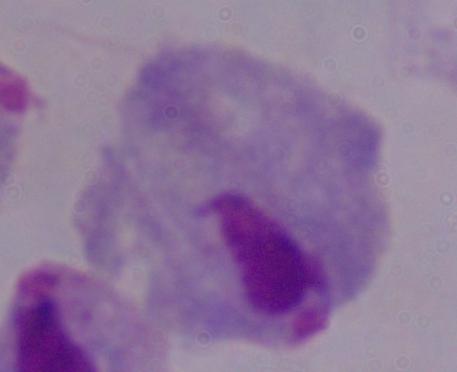 Micrograph. Captured at 1000x magnification. A trichomonad is shown.